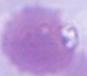

{
  "magnification": "1000x",
  "identification": "red blood cell",
  "modality": "micrograph"
}